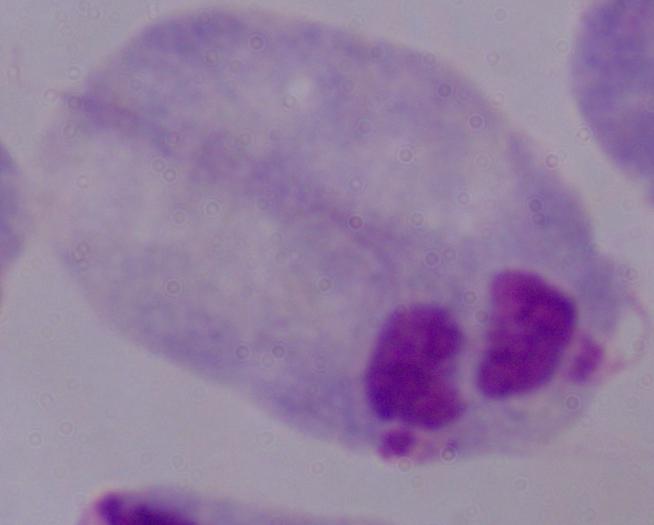
Captured at 1000x magnification. A trichomonad is seen. Micrograph.